Give the extent of all Trypanosoma brucei.
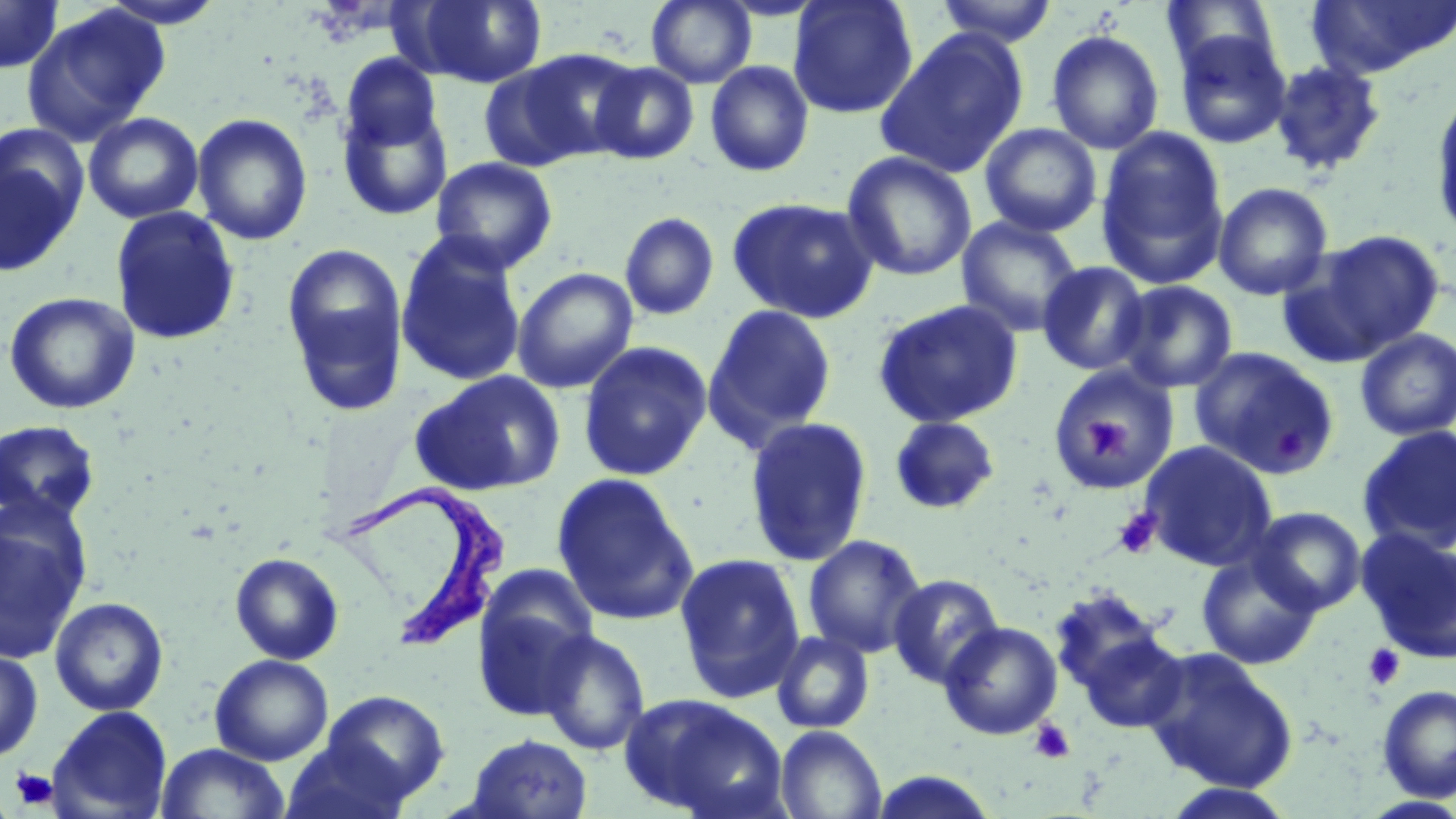
Approximate bounding boxes as [x1, y1, x2, y2] in pixels.
Trypanosoma brucei: [333, 479, 510, 650].

{
  "slide_level_diagnosis": "Trypanosoma brucei",
  "uninfected_red_blood_cell_locations": "approximate bounding boxes as [x1, y1, x2, y2] in pixels: [0, 0, 64, 74], [97, 0, 227, 29], [406, 0, 548, 88], [646, 0, 757, 88], [789, 0, 918, 119], [933, 0, 1059, 47], [1304, 0, 1456, 80], [1161, 1, 1282, 78], [22, 5, 169, 145], [1172, 28, 1292, 150], [876, 29, 1029, 178], [1046, 29, 1164, 155], [514, 48, 642, 161], [341, 53, 442, 150], [1269, 59, 1387, 177], [478, 60, 598, 172], [589, 61, 699, 164], [705, 61, 814, 177], [1430, 89, 1456, 246], [337, 100, 454, 222], [83, 111, 204, 225], [192, 113, 313, 246], [979, 123, 1102, 237], [1095, 127, 1230, 289], [0, 149, 83, 278], [841, 150, 978, 282], [429, 156, 558, 274], [1213, 181, 1333, 301], [726, 196, 880, 324], [110, 206, 241, 346], [618, 212, 719, 322], [956, 215, 1083, 337], [1296, 229, 1445, 361], [395, 232, 528, 388], [281, 242, 409, 417], [1036, 261, 1152, 376], [512, 267, 638, 394], [1114, 280, 1238, 394], [2, 291, 141, 415], [872, 298, 1025, 429], [702, 303, 838, 452], [1355, 328, 1456, 440], [578, 341, 712, 481], [1188, 347, 1341, 478], [1043, 365, 1179, 492], [411, 370, 565, 496], [888, 415, 1002, 515], [743, 416, 874, 567], [0, 419, 101, 525], [1357, 424, 1456, 556], [1139, 440, 1278, 571], [551, 473, 699, 625], [1248, 506, 1367, 615], [0, 508, 89, 665], [1356, 528, 1456, 665], [802, 534, 928, 658], [230, 552, 344, 665], [674, 552, 806, 703], [1197, 552, 1321, 670], [473, 567, 599, 712], [888, 573, 1005, 689], [1048, 586, 1174, 712], [49, 596, 169, 716], [940, 621, 1063, 740], [1073, 624, 1189, 736], [537, 629, 651, 756], [770, 630, 876, 734], [1140, 646, 1299, 793], [0, 648, 43, 764], [210, 654, 333, 765], [1376, 684, 1456, 802], [322, 691, 449, 802], [622, 693, 789, 818], [47, 706, 173, 819], [775, 725, 887, 819], [464, 733, 593, 818], [280, 738, 415, 819], [155, 742, 289, 819], [1159, 781, 1301, 818]",
  "magnification": "1000x",
  "stain": "May-Grünwald-Giemsa",
  "preparation": "thin blood smear",
  "platelet_locations": "approximate bounding boxes as [x1, y1, x2, y2] in pixels: [1079, 412, 1135, 460], [1274, 427, 1310, 467], [1113, 507, 1162, 559], [1363, 643, 1405, 690], [1029, 718, 1075, 763], [9, 767, 59, 812]",
  "field_of_view": "one of a larger specimen",
  "modality": "light microscopy",
  "image_size": "1456×819 pixels"
}